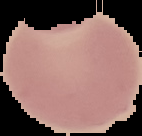

image type = segmented cell region with the area outside set to black
image size = 142×136 pixels
preparation = thin blood film
malaria status = uninfected